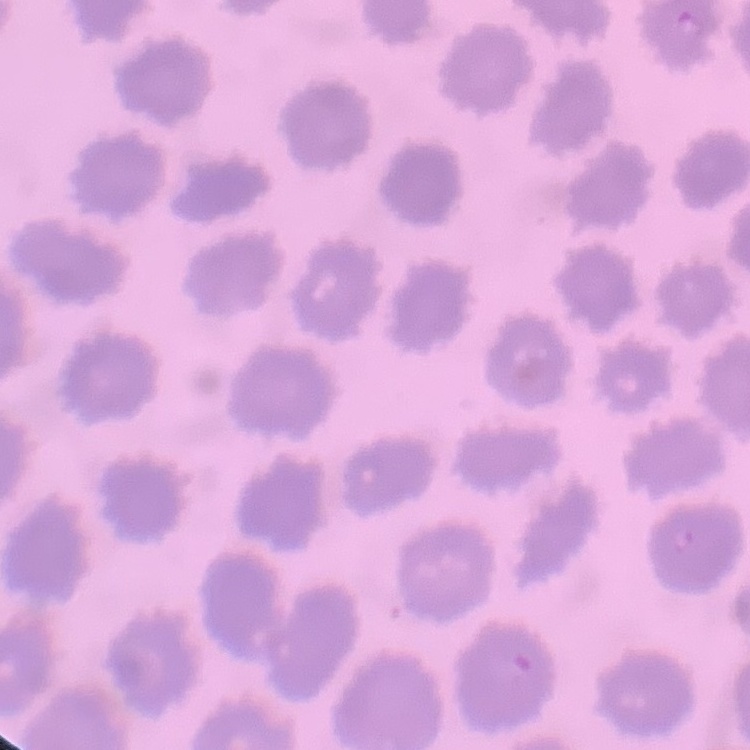

Summary:
  - Red blood cell morphology: no rouleaux formation
  - Preparation: thin blood film
  - Stain: Field's or Giemsa
  - Image type: one tile cut from a larger photomicrograph